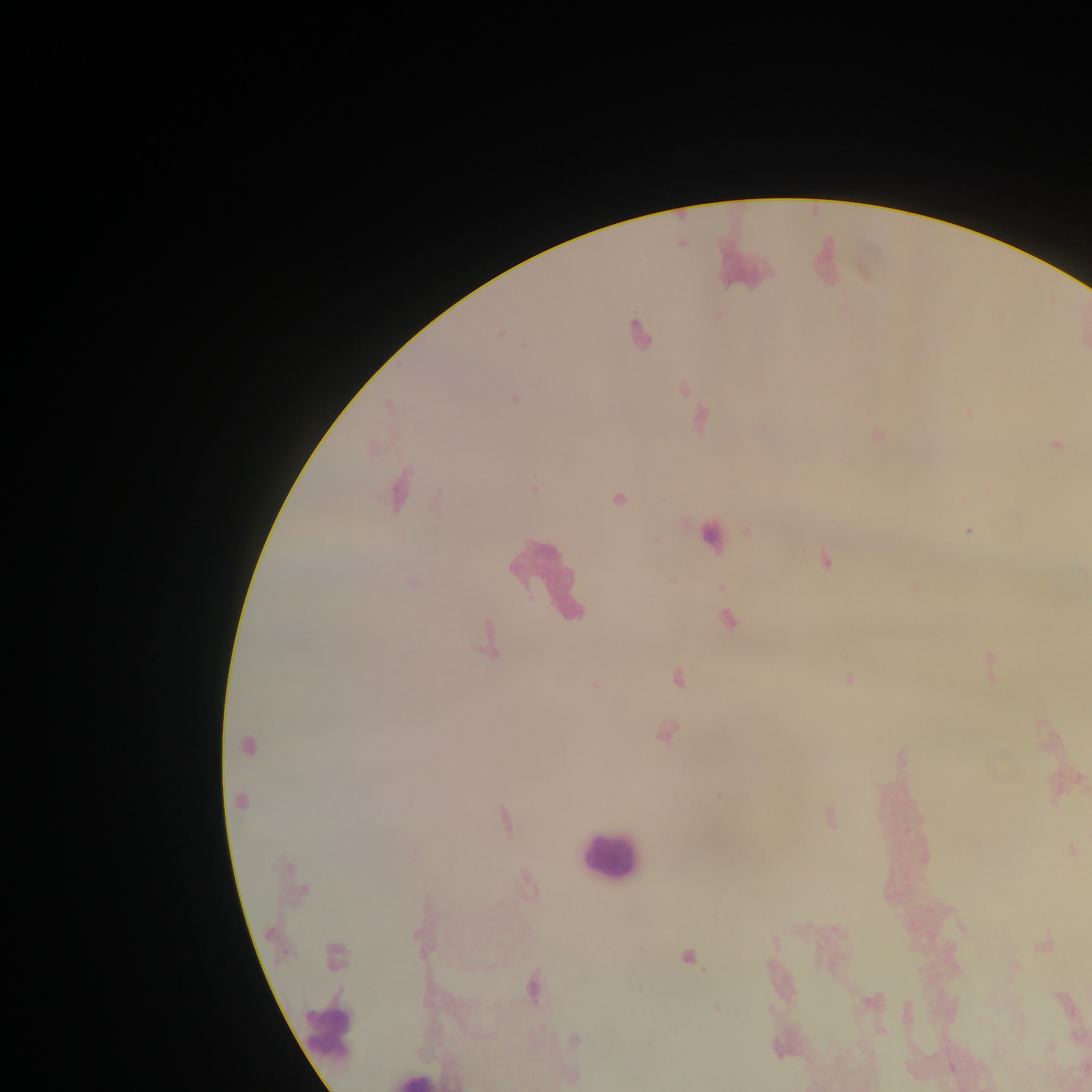

Approximate centers as x y in pixels. Malaria parasite locations: 500 334; 515 398; 1055 445; 397 492; 964 499; 618 500; 968 531; 826 560; 728 620; 488 641; 991 665; 677 679; 849 679; 596 684; 665 734; 248 746; 900 758; 240 802; 829 817; 503 820; 1072 849; 773 943; 1044 947; 335 957; 688 958; 532 988; 872 1002; 717 1008; 575 1040; 952 1067. Leukocyte locations: 741 252; 824 260; 710 535; 549 577; 609 854; 329 1029; 412 1080. Image is 1092×1092 pixels. Mobile-phone photograph taken through the microscope. Thick blood film. Sample from Ghana. One field of view.